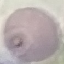
result = no malaria parasites seen
capture = smartphone through the microscope eyepiece
preparation = thin smear
image type = automatically extracted cell patch, resized to 64 × 64 pixels
stain = Giemsa